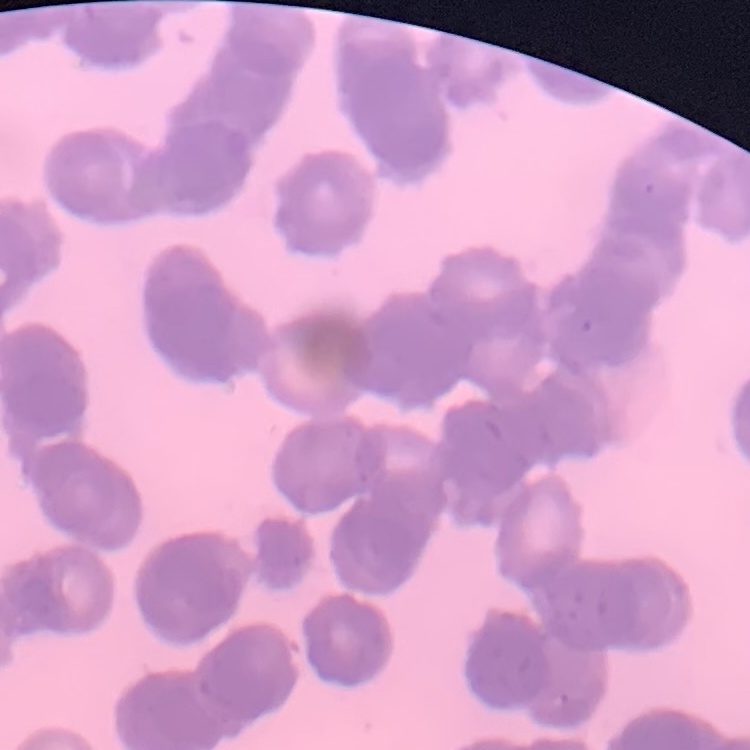
erythrocyte_morphology: rouleaux formation
image_type: square crop of a larger photomicrograph
stain: Field's or Giemsa
preparation: thin blood film